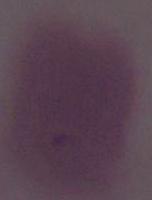

Captured at 1000x magnification. A red blood cell is shown. Micrograph.